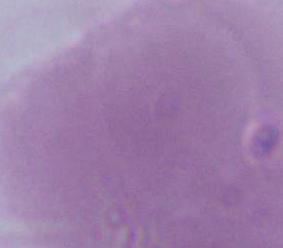
Summary:
  - Magnification: 1000x
  - Modality: micrograph
  - Identification: erythrocyte